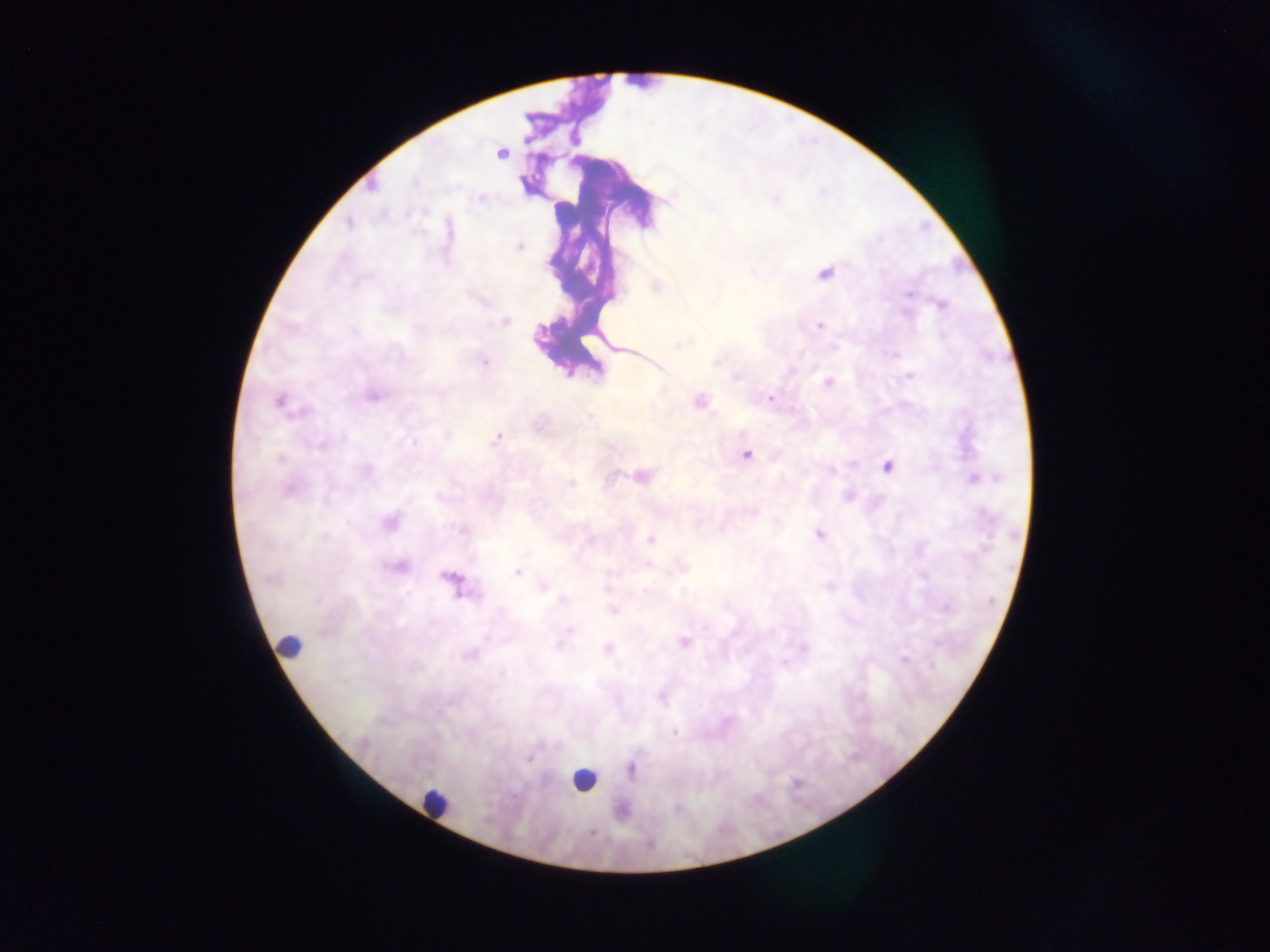

leukocyte locations = approximate centers as x y in pixels: 292 647; 583 780; 437 805
capture = mobile-phone photograph through a microscope
image size = 1270×952 pixels
Plasmodium parasite locations = approximate centers as x y in pixels: 908 294; 821 325; 909 377; 829 383; 770 398; 748 454; 887 465; 975 480; 818 534; 517 572; 783 664; 674 733
field of view = single
preparation = thick blood film
country = Ghana